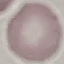
Summary:
  - Malaria status: uninfected
  - Stain: Giemsa
  - Capture: smartphone through the microscope eyepiece
  - Image type: automatically extracted cell patch, resized to 64 × 64 pixels
  - Preparation: thin blood film